Give the extent of all Plasmodium falciparum-infected red blood cells.
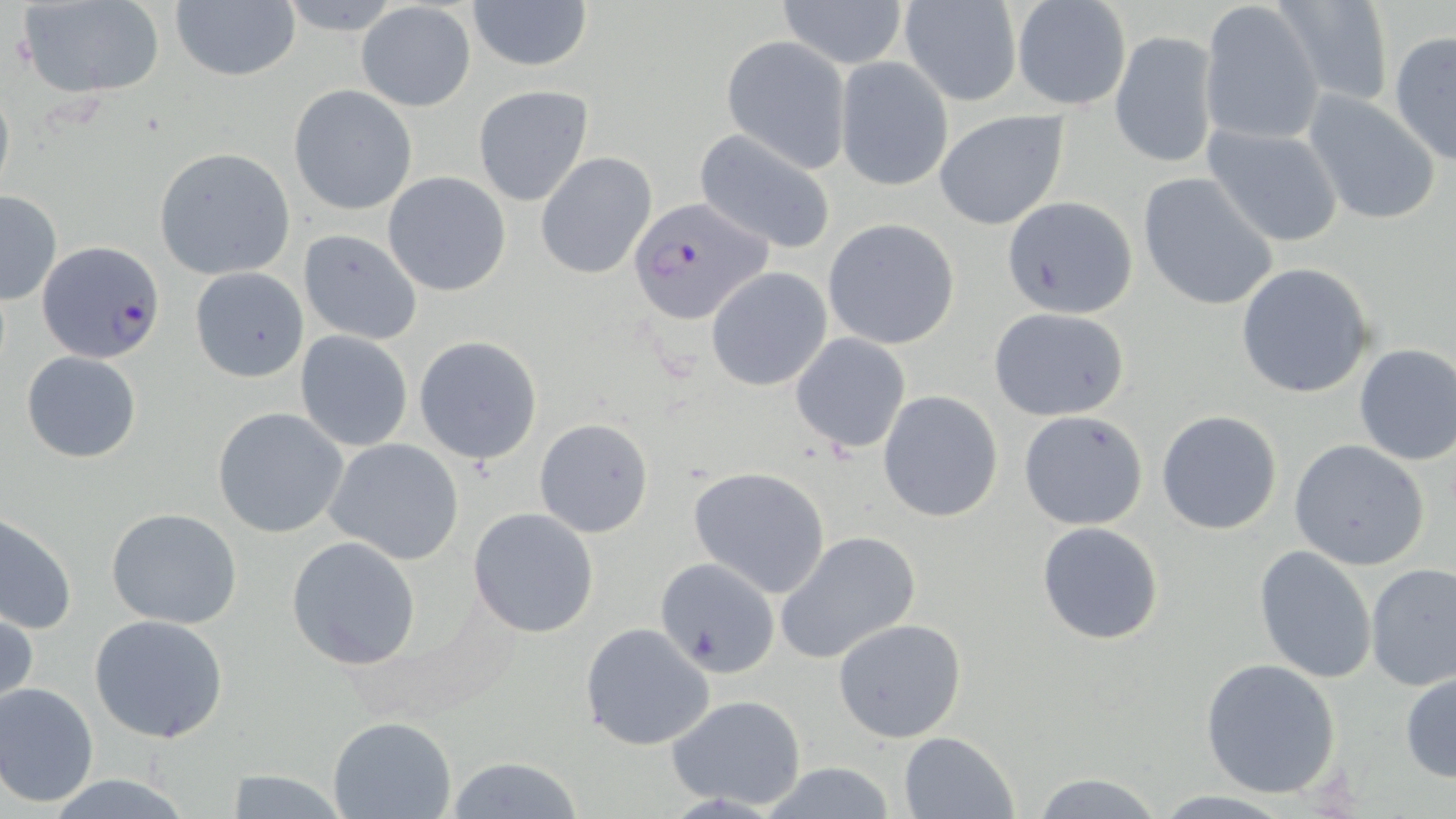

Approximate bounding boxes as [x1, y1, x2, y2] in pixels.
Plasmodium falciparum-infected red blood cells: [627, 196, 773, 327], [36, 241, 167, 364].

slide-level diagnosis = Plasmodium falciparum
magnification = 1000x
uninfected red blood cell locations = approximate bounding boxes as [x1, y1, x2, y2] in pixels: [466, 0, 594, 71], [776, 0, 910, 70], [1202, 0, 1326, 147], [1270, 0, 1393, 107], [169, 1, 301, 83], [1012, 1, 1131, 110], [17, 2, 164, 98], [355, 2, 477, 112], [898, 2, 1021, 107], [1110, 28, 1218, 170], [1388, 31, 1456, 165], [723, 36, 851, 171], [834, 58, 953, 191], [0, 78, 14, 202], [289, 85, 418, 216], [473, 85, 594, 206], [1304, 91, 1441, 226], [935, 110, 1068, 231], [1205, 124, 1345, 247], [694, 128, 839, 254], [153, 147, 297, 280], [534, 152, 658, 280], [381, 171, 511, 297], [1138, 172, 1280, 310], [1, 190, 63, 306], [1003, 195, 1139, 317], [823, 219, 960, 350], [299, 229, 423, 345], [1235, 262, 1378, 400], [706, 266, 833, 391], [189, 267, 308, 383], [987, 306, 1130, 421], [295, 331, 414, 450], [789, 333, 912, 454], [413, 335, 543, 464], [1352, 344, 1456, 466], [20, 351, 143, 463], [877, 390, 1004, 523], [211, 406, 349, 538], [1018, 410, 1149, 530], [1156, 410, 1284, 535], [533, 417, 654, 538], [323, 438, 464, 565], [1289, 440, 1429, 570], [688, 466, 831, 598], [106, 508, 243, 628], [467, 508, 599, 637], [0, 512, 77, 637], [1036, 522, 1165, 644], [775, 530, 922, 665], [286, 536, 423, 671], [1254, 546, 1378, 685], [651, 558, 781, 682], [1364, 563, 1456, 690], [1, 603, 37, 717], [88, 614, 229, 742], [831, 617, 967, 744], [579, 622, 717, 751], [1201, 658, 1342, 799], [1401, 669, 1456, 782], [0, 681, 100, 807], [664, 694, 809, 808], [327, 716, 457, 819], [898, 731, 1019, 818], [444, 757, 588, 817], [755, 762, 903, 819], [218, 767, 348, 818], [1029, 770, 1170, 819], [45, 774, 195, 818]
modality = light microscopy
field of view = single
stain = May-Grünwald-Giemsa
preparation = thin blood smear
image size = 1456×819 pixels